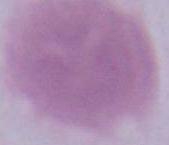 Captured at 1000x magnification. Micrograph. An erythrocyte is seen.